Locate every Plasmodium parasite.
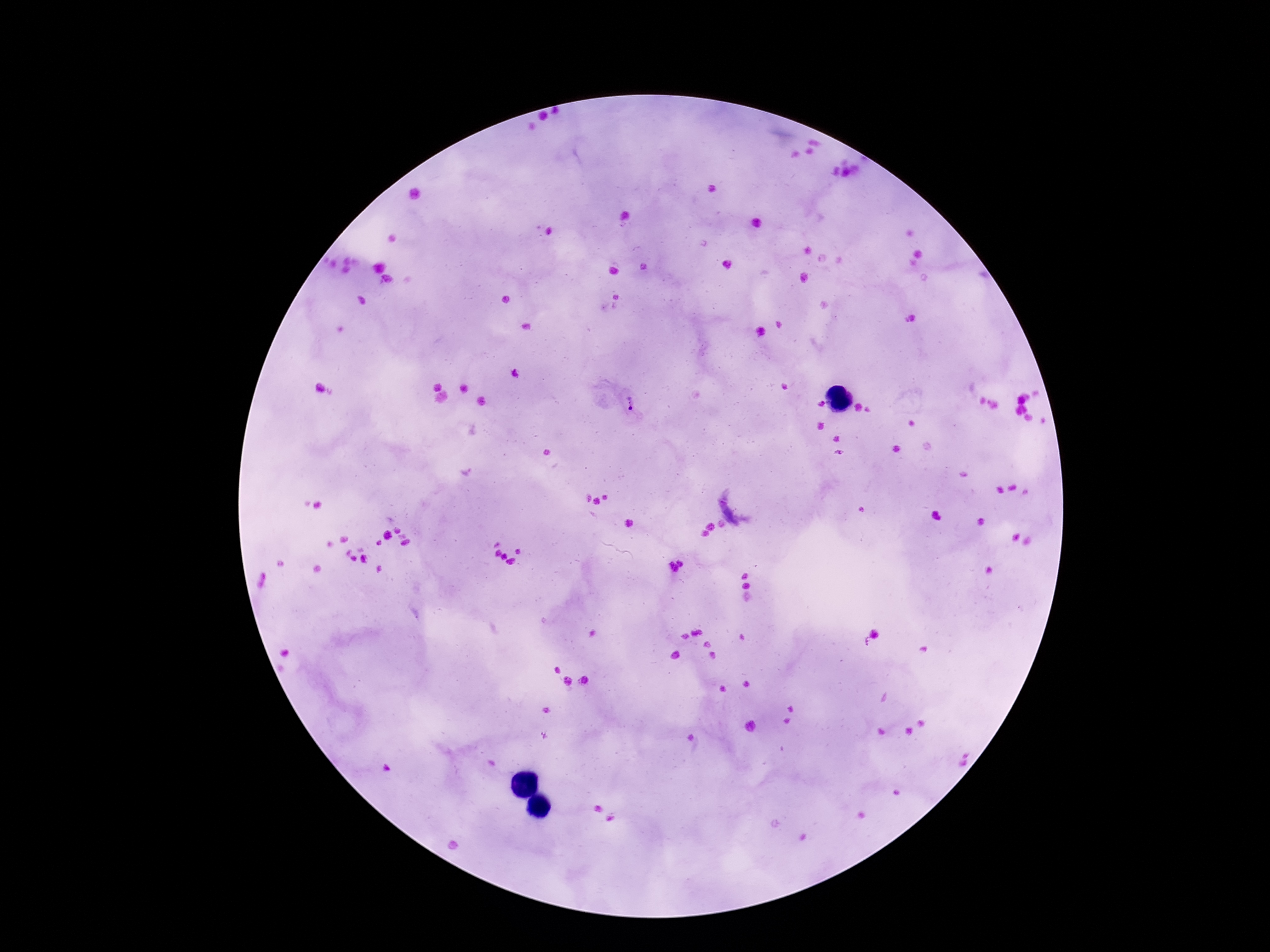
Approximate centers as (x, y) in pixels.
Plasmodium parasites: (630, 405).

preparation = thick blood smear
capture = smartphone camera through the microscope eyepiece
magnification = 100x
patient malaria status = positive
stain = Giemsa
field of view = one from this slide
image size = 1270×952 pixels